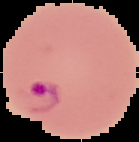

Summary:
  - Image size: 139×142 pixels
  - Image type: cell region segmented out of the field of view; surrounding area masked to black
  - Preparation: thin blood film
  - Result: Plasmodium parasites detected